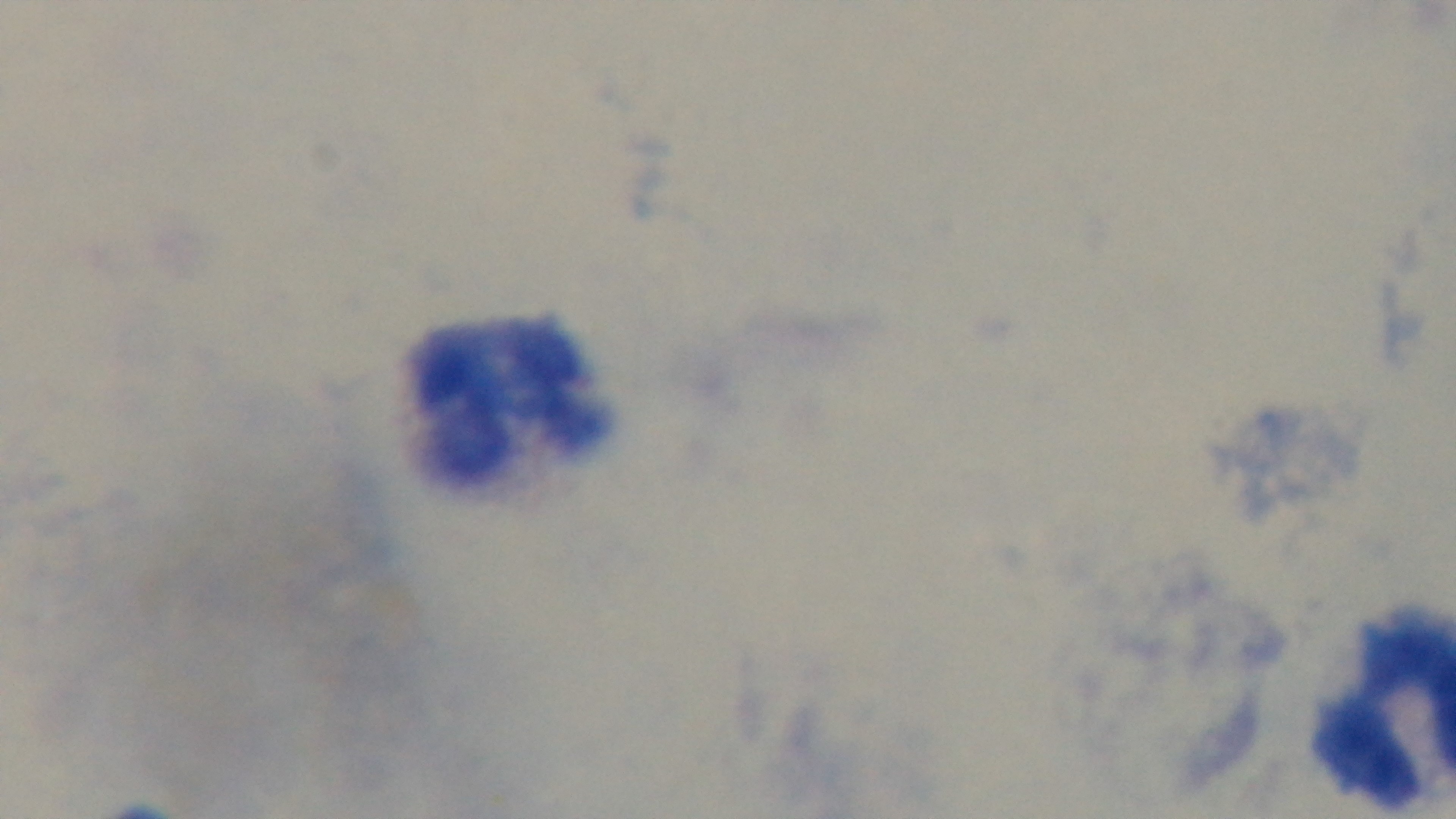
{
  "modality": "light microscopy",
  "objective": "100x oil immersion",
  "preparation": "thick blood film",
  "stain": "Giemsa",
  "capture": "mounted 4K digital camera",
  "malaria_status": "uninfected",
  "field_of_view": "one from the slide"
}